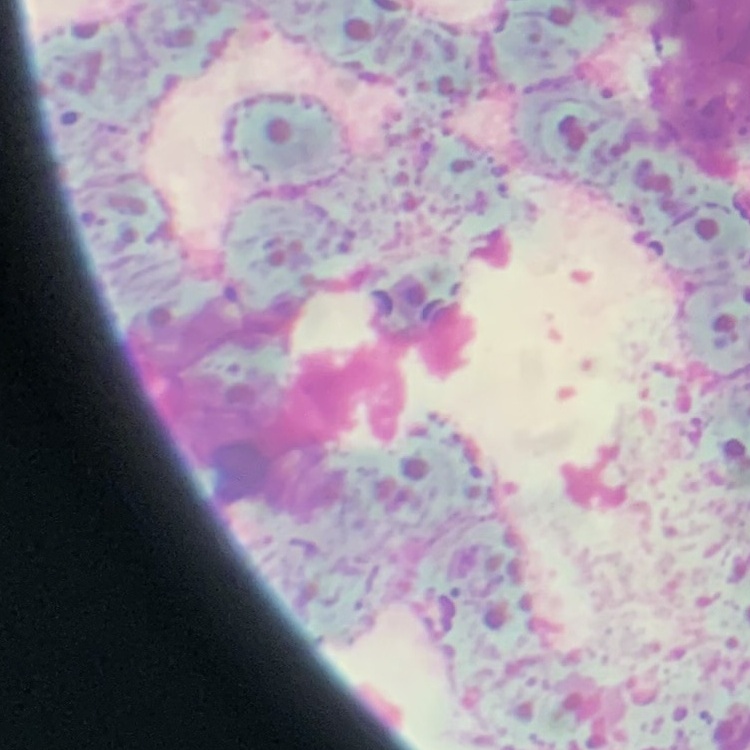

{
  "erythrocyte_morphology": "rouleaux formation",
  "preparation": "thin peripheral smear",
  "stain": "Field's or Giemsa",
  "image_type": "square crop of a larger photomicrograph"
}